Assess this cell for malaria.
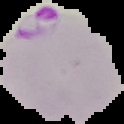
It is parasitized.

Summary:
  - Image size: 124×124 pixels
  - Image type: cell region segmented out of the field of view; surrounding area masked to black
  - Preparation: thin blood smear